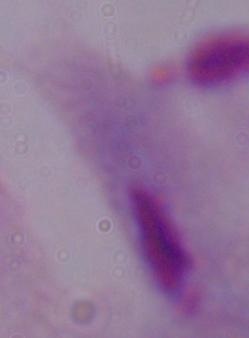
Captured at 1000x magnification. Micrograph. A trichomonad is seen.